Assess this cell for malaria.
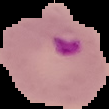
Parasitized.

preparation = thin blood film
image type = segmented cell region with the area outside set to black
image size = 109×109 pixels